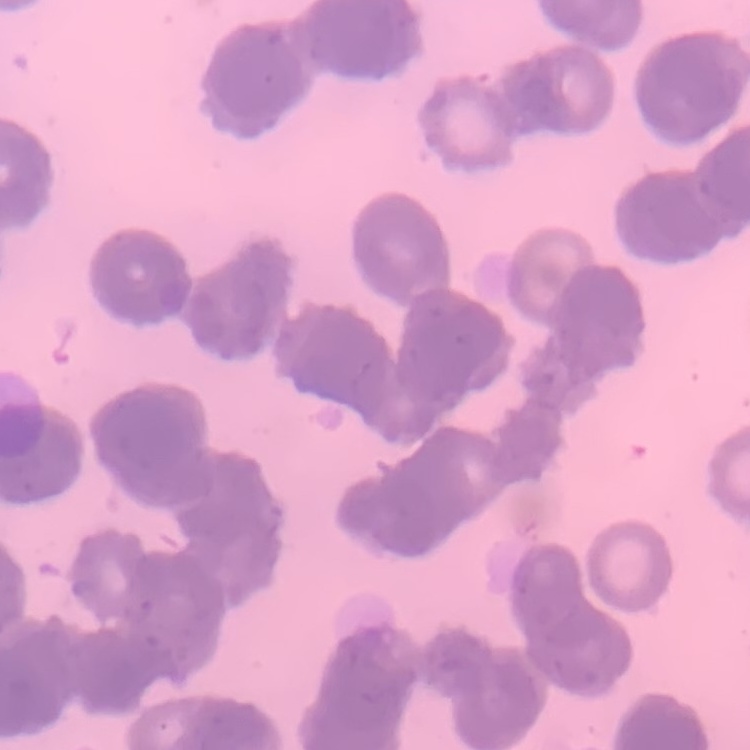
Summary:
  - Red blood cell morphology: rouleaux formation
  - Stain: Field's or Giemsa
  - Preparation: thin blood film
  - Image type: one tile cut from a larger photomicrograph